State which parasite is depicted.
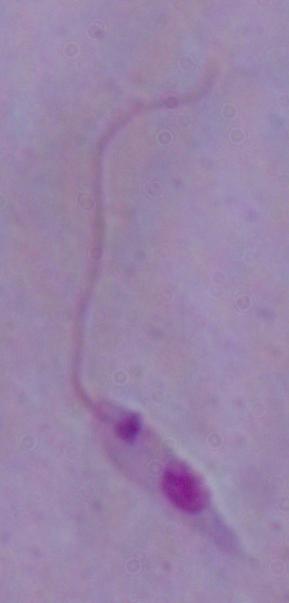
This is Leishmania.

Summary:
  - Modality: photomicrograph
  - Magnification: 1000x